Assess this cell for malaria.
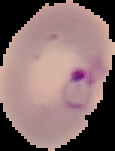
Parasitized.

Summary:
  - Preparation: thin blood film
  - Image size: 115×151 pixels
  - Image type: cell region segmented out of the field of view; surrounding area masked to black